Describe the morphology of the erythrocytes.
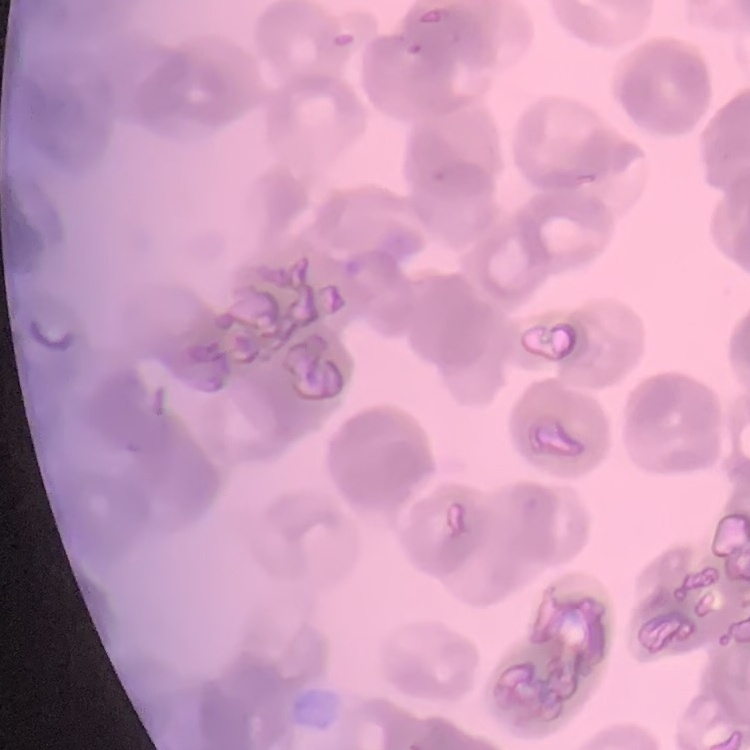
Rouleaux formation.

preparation = thin peripheral smear
stain = Field's or Giemsa
image type = one tile cut from a larger photomicrograph